Point out each malaria parasite and each leukocyte.
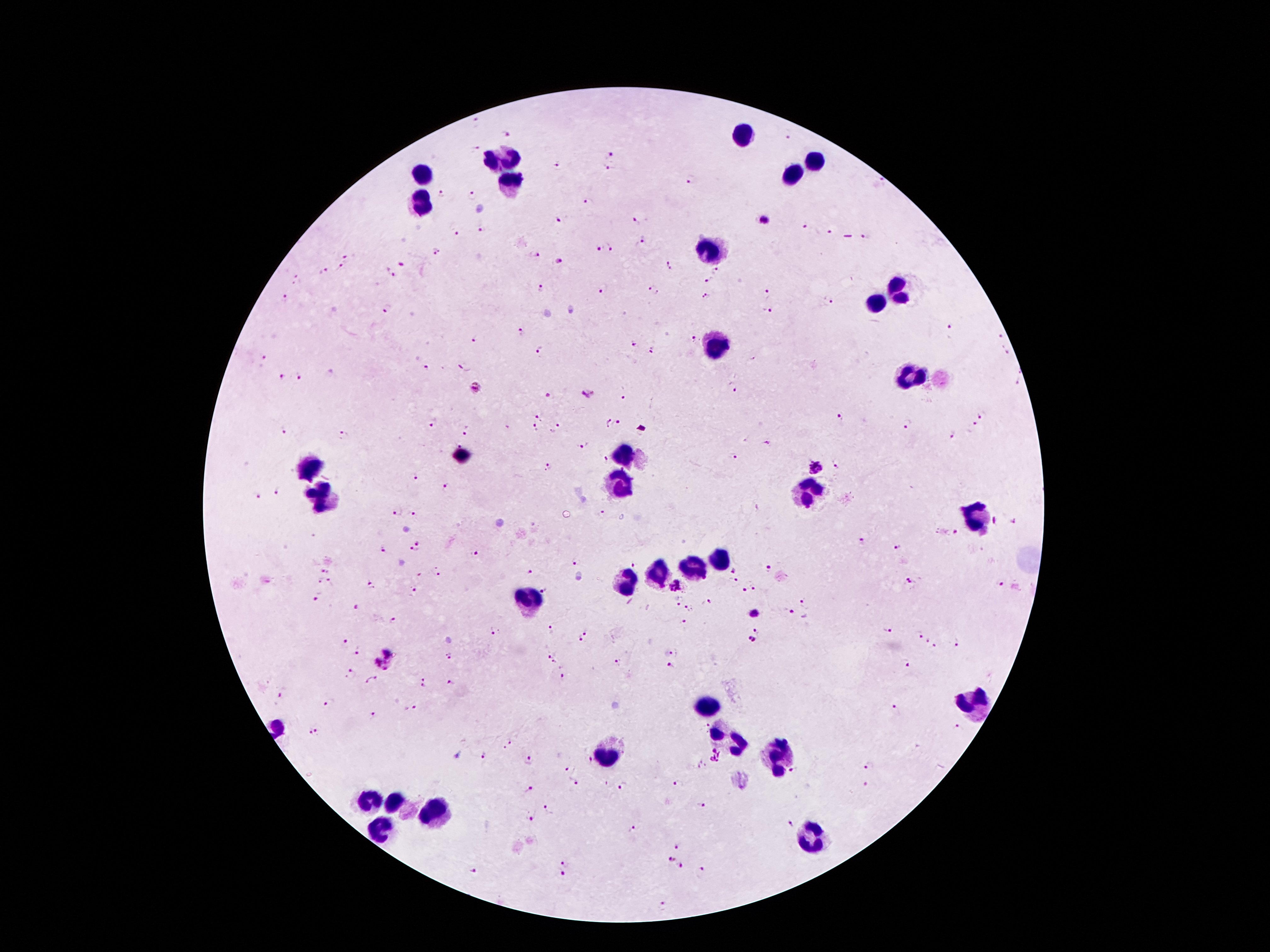
Approximate object centers, in pixels from the top-left corner.
Malaria parasites: (x=475, y=122), (x=508, y=134), (x=788, y=136), (x=477, y=149), (x=607, y=154), (x=557, y=165), (x=607, y=170), (x=692, y=180), (x=440, y=193), (x=471, y=196), (x=587, y=201), (x=560, y=219), (x=636, y=221), (x=763, y=222), (x=803, y=226), (x=481, y=229), (x=828, y=232), (x=457, y=233), (x=866, y=237), (x=643, y=241), (x=608, y=248), (x=597, y=249), (x=436, y=252), (x=347, y=256), (x=535, y=256), (x=556, y=261), (x=402, y=265), (x=669, y=265), (x=341, y=268), (x=718, y=270), (x=324, y=271), (x=391, y=274), (x=298, y=279), (x=710, y=280), (x=541, y=287), (x=603, y=289), (x=651, y=291), (x=766, y=291), (x=706, y=295), (x=286, y=299), (x=828, y=302), (x=386, y=309), (x=765, y=312), (x=950, y=327), (x=522, y=331), (x=1001, y=337), (x=692, y=338), (x=477, y=339), (x=634, y=343), (x=540, y=350), (x=652, y=351), (x=262, y=358), (x=465, y=366), (x=426, y=368), (x=282, y=377), (x=300, y=377), (x=475, y=387), (x=732, y=387), (x=588, y=393), (x=549, y=395), (x=624, y=398), (x=540, y=416), (x=982, y=416), (x=840, y=417), (x=431, y=421), (x=606, y=422), (x=973, y=423), (x=618, y=424), (x=908, y=425), (x=557, y=428), (x=535, y=429), (x=467, y=430), (x=286, y=432), (x=344, y=435), (x=953, y=436), (x=460, y=443), (x=767, y=443), (x=583, y=445), (x=734, y=456), (x=605, y=460), (x=815, y=466), (x=837, y=467), (x=546, y=468), (x=623, y=469), (x=416, y=477), (x=447, y=488), (x=278, y=489), (x=257, y=496), (x=395, y=513), (x=603, y=514), (x=414, y=515), (x=1014, y=522), (x=955, y=533), (x=862, y=540), (x=417, y=543), (x=897, y=547), (x=382, y=550), (x=414, y=551), (x=475, y=554), (x=576, y=561), (x=634, y=564), (x=769, y=569), (x=325, y=571), (x=734, y=571), (x=530, y=572), (x=437, y=574), (x=320, y=581), (x=911, y=581), (x=331, y=582), (x=733, y=582), (x=677, y=584), (x=1002, y=584), (x=371, y=585), (x=754, y=586), (x=414, y=589), (x=545, y=590), (x=745, y=590), (x=318, y=594), (x=680, y=601), (x=707, y=602), (x=804, y=602), (x=355, y=608), (x=689, y=608), (x=792, y=612), (x=753, y=613), (x=394, y=621), (x=685, y=622), (x=552, y=629), (x=494, y=630), (x=888, y=630), (x=586, y=631), (x=918, y=635), (x=579, y=639), (x=751, y=639), (x=928, y=641), (x=957, y=641), (x=344, y=644), (x=934, y=645), (x=389, y=651), (x=676, y=651), (x=360, y=652), (x=450, y=654), (x=548, y=656), (x=554, y=661), (x=618, y=662), (x=906, y=662), (x=671, y=666), (x=380, y=668), (x=351, y=674), (x=563, y=675), (x=425, y=677), (x=369, y=681), (x=453, y=682), (x=424, y=687), (x=282, y=693), (x=330, y=702), (x=414, y=706), (x=894, y=709), (x=374, y=715), (x=959, y=729), (x=318, y=730), (x=309, y=733), (x=508, y=744), (x=714, y=754), (x=483, y=755), (x=588, y=760), (x=528, y=761), (x=869, y=767), (x=565, y=769), (x=792, y=771), (x=574, y=783), (x=866, y=784), (x=678, y=785), (x=623, y=787), (x=528, y=790), (x=700, y=804), (x=549, y=809), (x=531, y=818), (x=790, y=824), (x=632, y=828), (x=678, y=846), (x=671, y=860), (x=564, y=862), (x=681, y=866), (x=703, y=868), (x=471, y=870), (x=564, y=875), (x=661, y=905).
Leukocytes: (x=743, y=138), (x=504, y=158), (x=815, y=162), (x=791, y=172), (x=423, y=173), (x=509, y=185), (x=420, y=202), (x=713, y=254), (x=901, y=289), (x=880, y=304), (x=712, y=347), (x=913, y=378), (x=623, y=457), (x=464, y=458), (x=310, y=466), (x=619, y=485), (x=809, y=493), (x=323, y=496), (x=975, y=516), (x=720, y=559), (x=693, y=569), (x=659, y=573), (x=626, y=582), (x=527, y=600), (x=710, y=705), (x=977, y=706), (x=730, y=737), (x=779, y=757), (x=606, y=758), (x=371, y=801), (x=399, y=805), (x=433, y=816), (x=382, y=827), (x=814, y=841).

Smartphone photograph taken through the microscope eyepiece. Patient malaria status: infected with Plasmodium falciparum. Giemsa stain. Thick blood film. 100x magnification. Image is 1270×952 pixels. Single field of view.